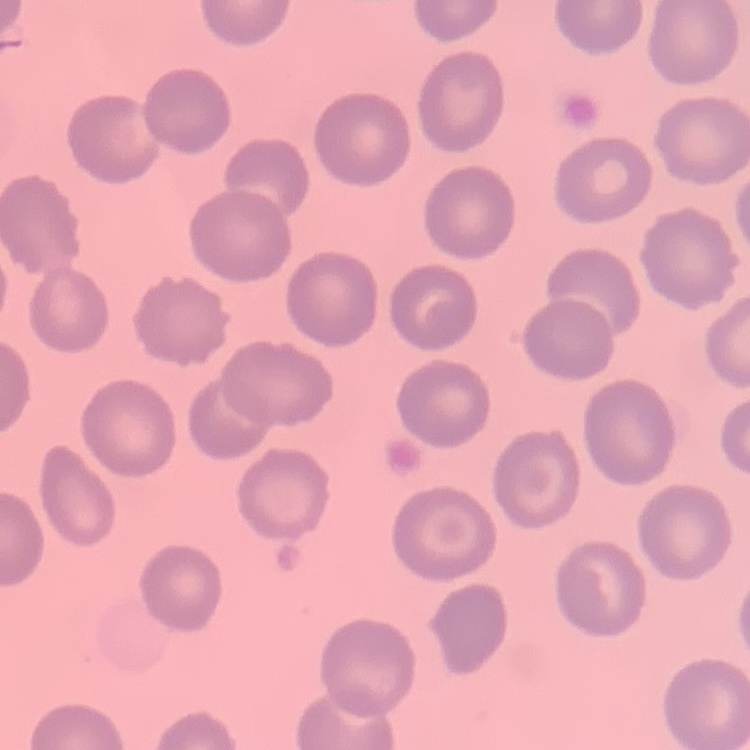 The red blood cells show no rouleaux formation. One tile cut from a larger photomicrograph. Thin blood film. Field's or Giemsa stain.